Classify this cell by malaria status.
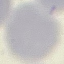
Uninfected.

Automatically extracted cell patch, resized to 64 × 64 pixels. Acquired by smartphone through the microscope eyepiece. Giemsa stain. Thin blood film.